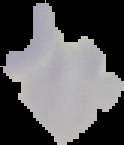

Malaria status: uninfected. From a thin blood smear. Image is 124×145 pixels. Cell region segmented out of the field of view; the surrounding area is masked to black.